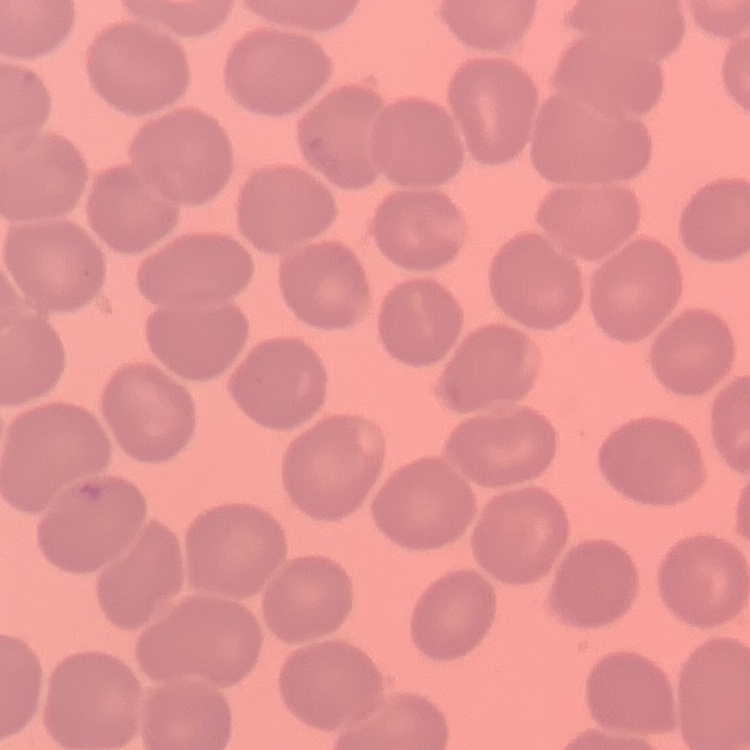
Summary:
  - Erythrocyte morphology: no rouleaux formation
  - Image type: square crop of a larger photomicrograph
  - Stain: Field's or Giemsa
  - Preparation: thin peripheral smear